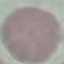

Result: no malaria parasites seen. Cell patch, automatically extracted from a larger field of view and resized to 64 × 64 pixels. Giemsa-stained preparation. Thin smear of blood. Photographed with a smartphone camera at the microscope eyepiece.